Point out each Plasmodium parasite.
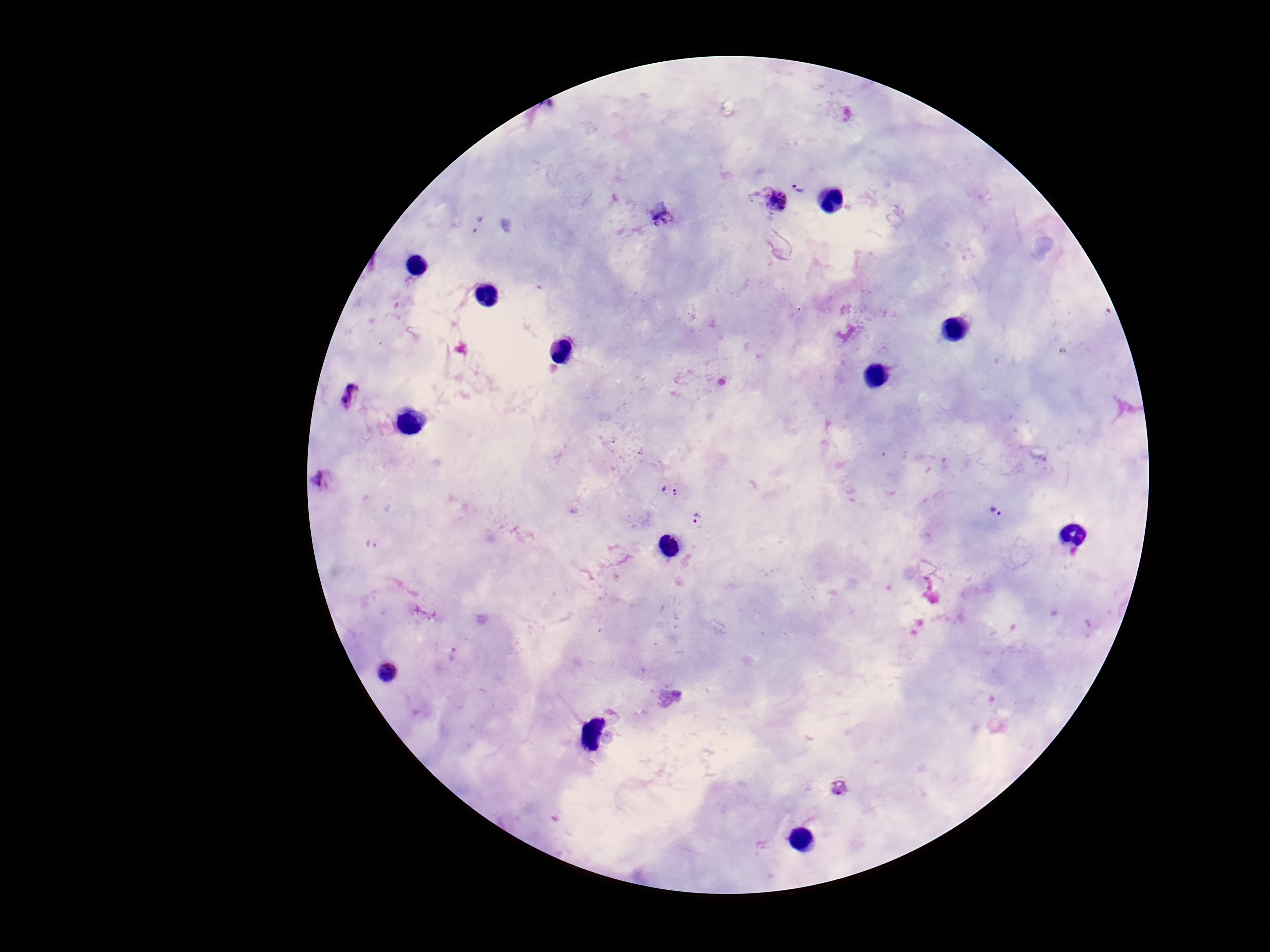

Approximate object centers, in pixels from the top-left corner.
Plasmodium parasites: (x=801, y=185), (x=770, y=198), (x=662, y=217), (x=477, y=223), (x=349, y=398), (x=325, y=482), (x=669, y=490), (x=994, y=512), (x=699, y=520), (x=371, y=543), (x=387, y=672), (x=839, y=787).

Summary:
  - Magnification: 100x
  - Preparation: thick blood film
  - Field of view: one from this slide
  - Capture: smartphone camera through the microscope eyepiece
  - Image size: 1270×952 pixels
  - Stain: Giemsa
  - Patient malaria status: positive